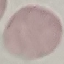
malaria status = uninfected
image type = automatically extracted cell patch, resized to 64 × 64 pixels
capture = smartphone through the microscope eyepiece
preparation = thin smear
stain = Giemsa